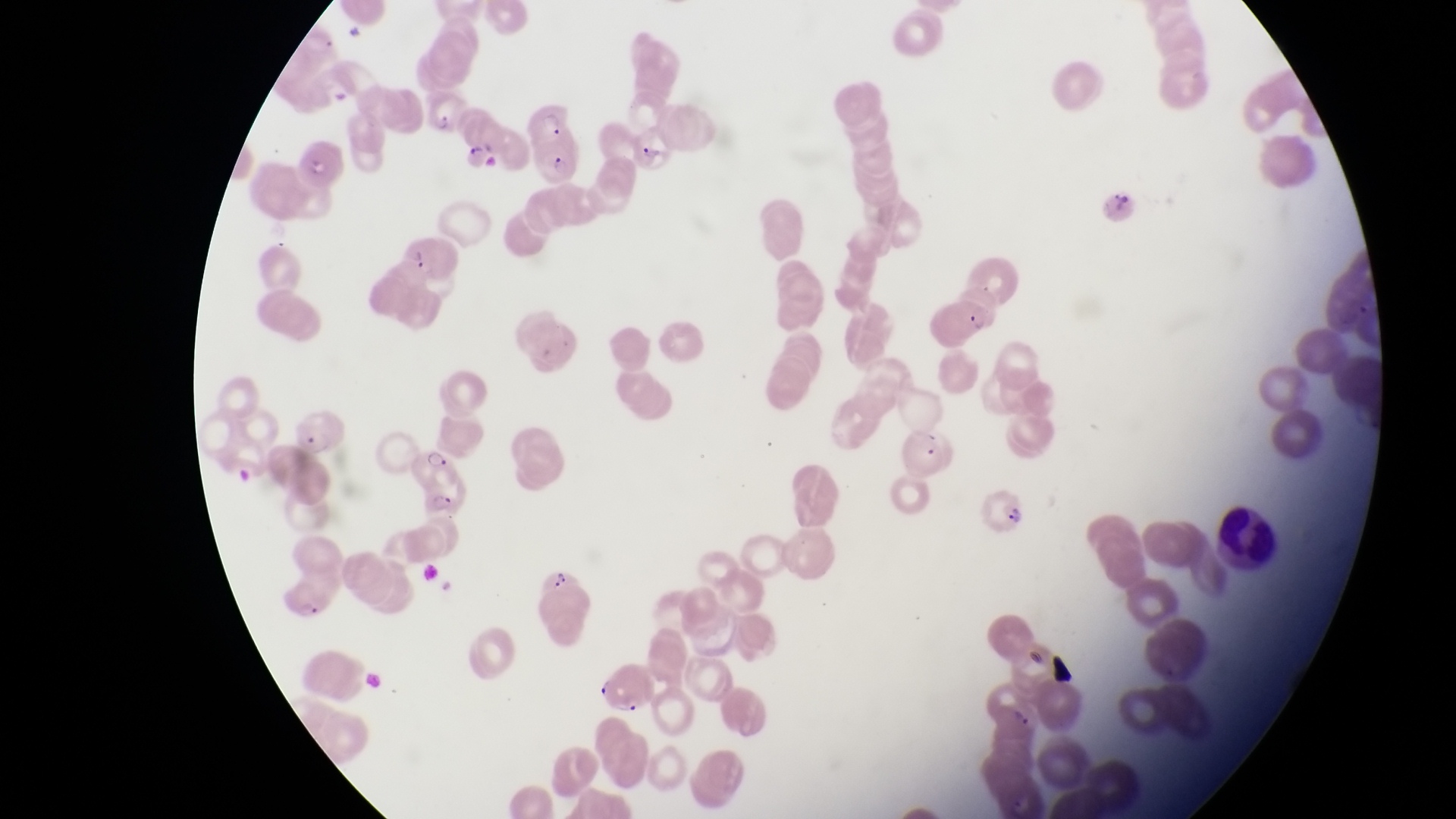

Approximate bounding boxes as [left, top, right, bottom] in pixels.
Summary:
  - Parasitised red blood cell locations: [429, 93, 476, 136], [522, 95, 572, 148], [632, 129, 677, 179], [462, 132, 507, 178], [536, 139, 581, 184], [294, 142, 343, 187], [388, 221, 444, 280], [933, 291, 989, 343], [407, 444, 456, 491], [422, 488, 475, 527], [973, 491, 1029, 538], [541, 563, 583, 603], [278, 574, 339, 621], [597, 664, 658, 714], [980, 686, 1043, 742]
  - Leukocyte locations: [1212, 499, 1279, 572]
  - Artifact (platelet-like body, stain precipitate, or debris) locations: [1110, 188, 1134, 215]
  - Country: Uganda
  - Magnification: 1000x
  - Preparation: thin blood film
  - Capture: smartphone photograph through the eyepiece of an Olympus CX-23 microscope
  - Field of view: single
  - Image size: 1456×819 pixels